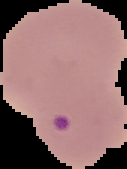
image size = 127×169 pixels
malaria status = parasitized
preparation = thin blood smear
image type = segmented cell region on a black background